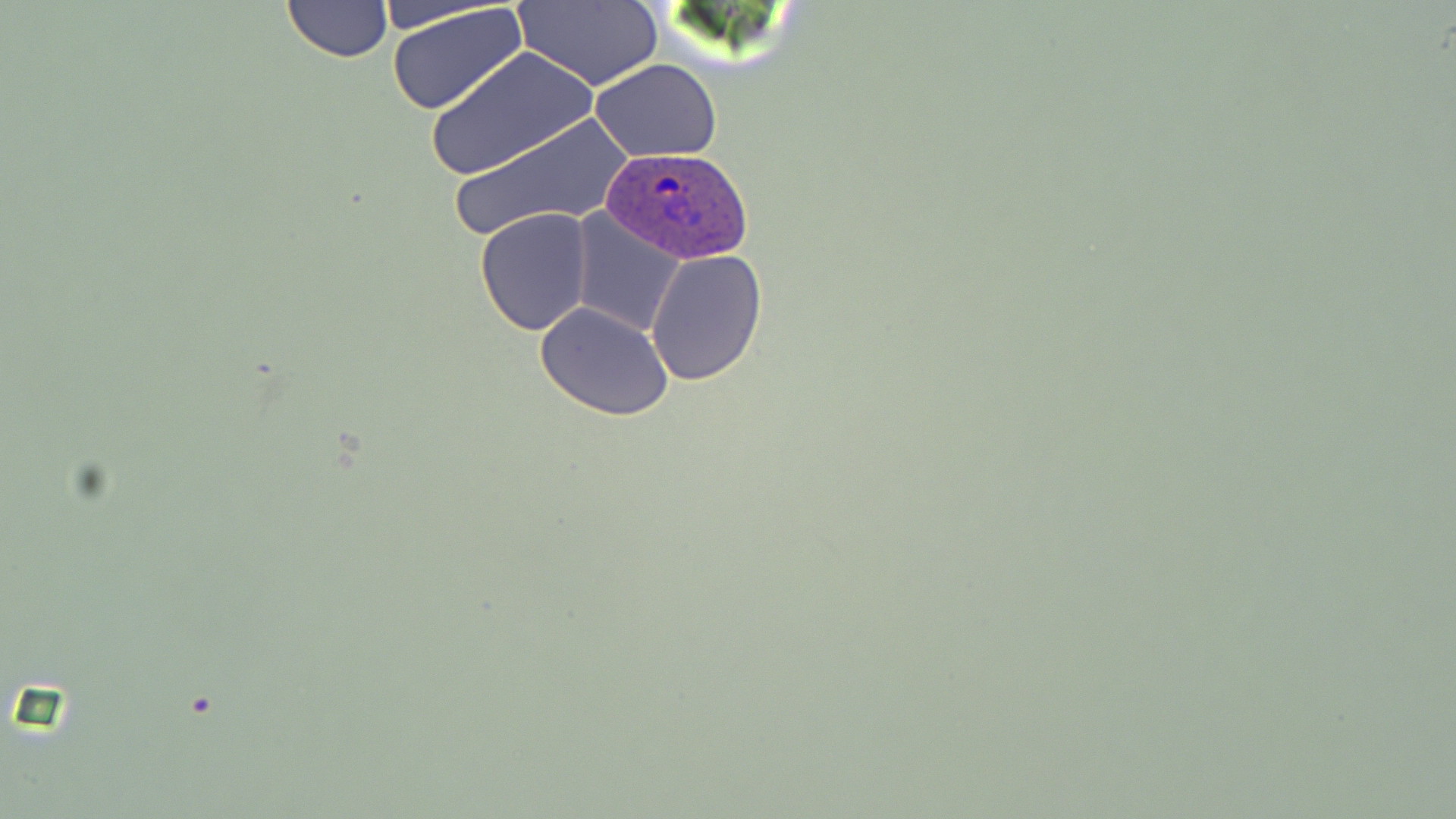

Summary:
  - Coordinate format: approximate bounding boxes as (x1, y1, x2, y2) in pixels
  - Uninfected red blood cell locations: (280, 1, 392, 63), (513, 1, 662, 89), (385, 2, 530, 117), (428, 46, 596, 181), (590, 59, 723, 163), (447, 111, 637, 240), (475, 208, 593, 334), (571, 211, 686, 337), (645, 249, 768, 386), (535, 302, 677, 422)
  - Plasmodium ovale-infected red blood cell locations: (598, 145, 756, 266)
  - Slide-level diagnosis: Plasmodium ovale
  - Field of view: one of a larger specimen
  - Modality: optical microscopy
  - Magnification: 1000x
  - Stain: May-Grünwald-Giemsa
  - Image size: 1456×819 pixels
  - Preparation: thin blood smear